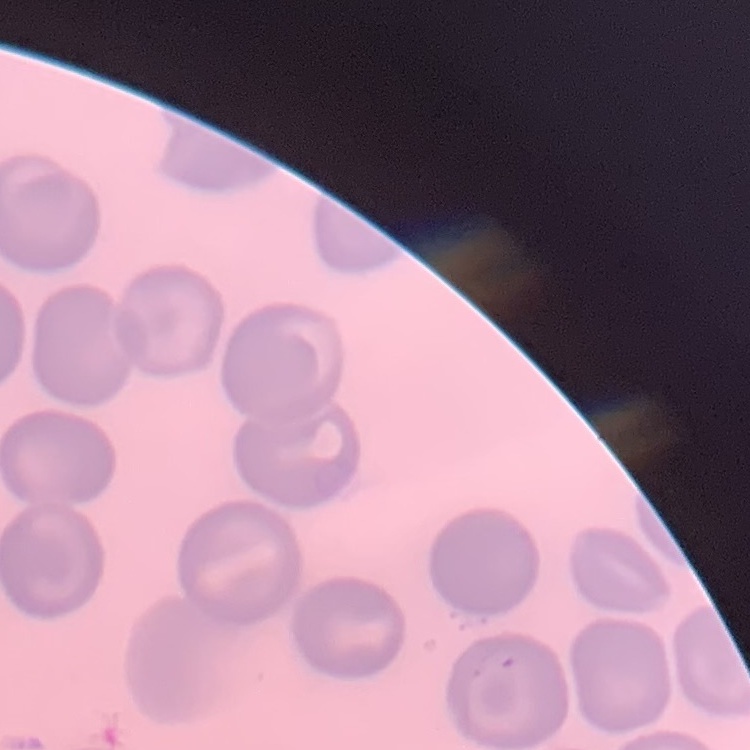

erythrocyte_morphology: no rouleaux formation
preparation: thin blood smear
image_type: square crop of a larger photomicrograph
stain: Field's or Giemsa